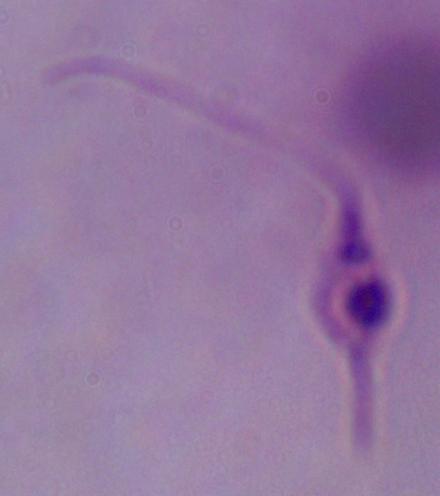

modality = photomicrograph
magnification = 1000x
identification = Leishmania